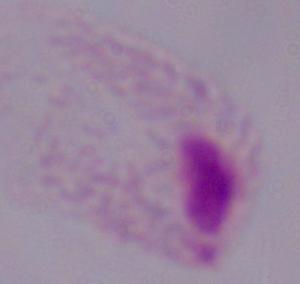
Summary:
  - Magnification: 1000x
  - Modality: micrograph
  - Identification: trichomonad